Classify this cell by malaria status.
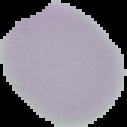
Uninfected.

image size = 127×127 pixels
preparation = thin blood film
image type = segmented cell region with the area outside set to black